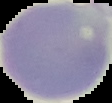
Segmented cell region on a black background. Image is 112×103 pixels. From a thin blood smear. Malaria status: uninfected.